Locate every blood parasite and identify its species.
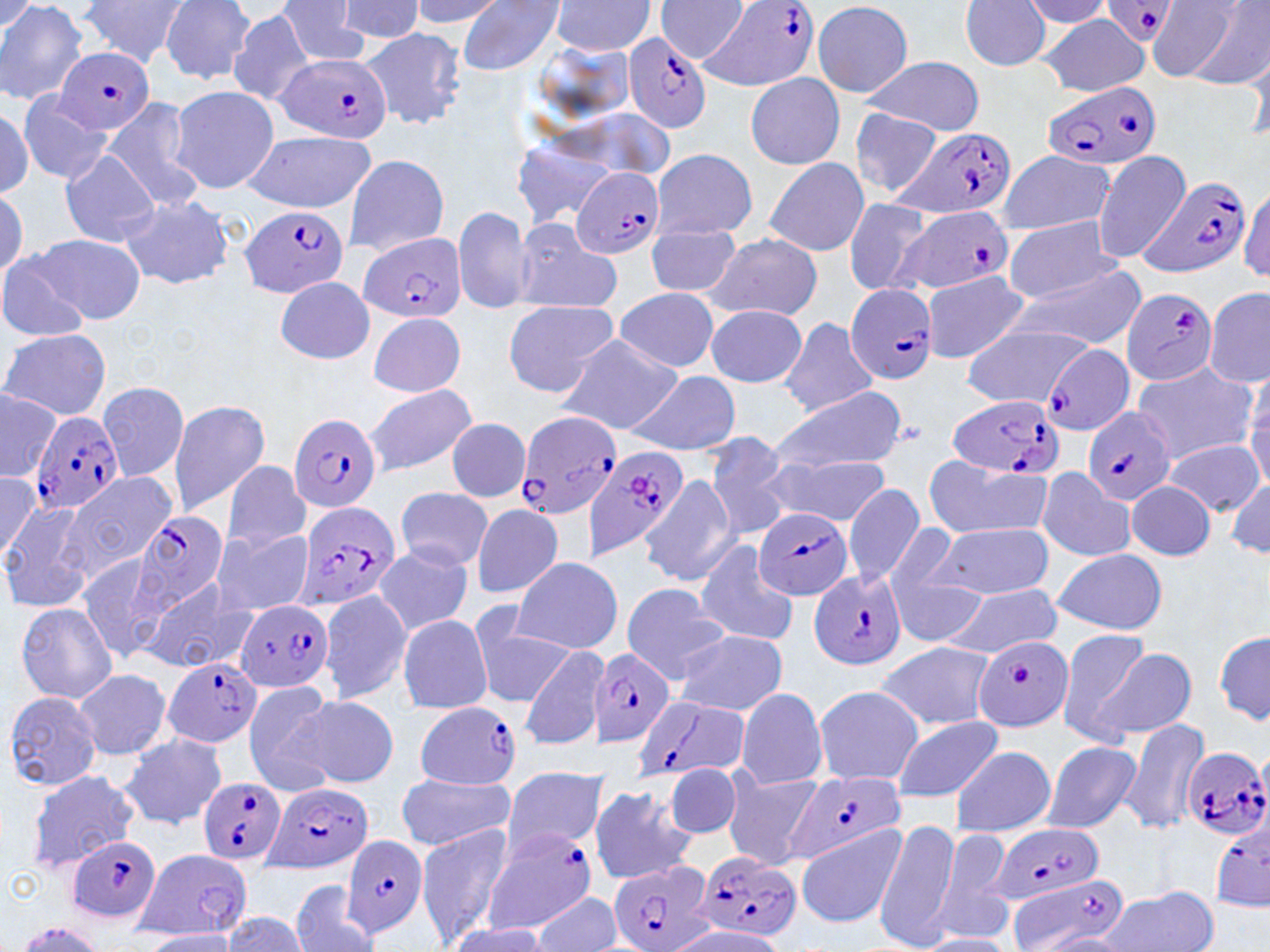

Approximate bounding boxes as [x1, y1, x2, y2] in pixels.
Plasmodium falciparum-infected red blood cells (subset): [697, 0, 821, 92], [1099, 1, 1182, 45], [624, 33, 714, 136], [57, 47, 153, 136], [277, 51, 391, 143], [1041, 83, 1161, 173], [894, 125, 1016, 221], [571, 165, 665, 260], [1141, 177, 1251, 278], [241, 204, 346, 298], [899, 205, 1015, 295], [357, 233, 466, 323], [1121, 289, 1217, 385], [1042, 343, 1135, 435], [947, 394, 1066, 479], [1082, 404, 1175, 506], [513, 409, 623, 522], [28, 412, 124, 517], [288, 413, 381, 515], [581, 446, 691, 559], [290, 500, 401, 614], [756, 507, 852, 601], [128, 509, 230, 611], [807, 568, 907, 673], [234, 600, 331, 692], [974, 636, 1074, 732], [590, 649, 674, 747], [164, 657, 264, 748], [634, 695, 747, 783], [416, 701, 524, 790], [1181, 748, 1270, 840], [788, 772, 910, 861], [196, 777, 288, 865], [263, 781, 375, 874], [1210, 819, 1270, 910], [485, 825, 602, 932], [985, 825, 1105, 905], [64, 834, 162, 924], [341, 835, 429, 938], [136, 848, 253, 940], [689, 850, 803, 942], [609, 857, 716, 952], [1008, 875, 1131, 951].
No Plasmodium ovale, Plasmodium malariae, Plasmodium vivax, Babesia divergens, or Trypanosoma brucei observed.

Uninfected red blood cell locations (subset): [0, 0, 37, 41], [82, 0, 193, 66], [407, 0, 508, 30], [458, 0, 565, 73], [551, 0, 657, 57], [1015, 0, 1116, 31], [1147, 0, 1237, 82], [0, 1, 90, 105], [160, 1, 256, 83], [271, 1, 373, 65], [339, 1, 425, 44], [658, 1, 749, 65], [812, 1, 913, 98], [1188, 1, 1270, 90], [958, 2, 1054, 72], [227, 8, 317, 108], [1037, 14, 1151, 95], [358, 27, 468, 131], [1244, 43, 1270, 145], [861, 57, 988, 135], [745, 72, 845, 170], [167, 86, 279, 193], [18, 91, 113, 184], [100, 96, 201, 205], [0, 107, 33, 195], [552, 107, 676, 179], [850, 108, 945, 197], [244, 131, 377, 214], [512, 136, 621, 227], [649, 148, 758, 240], [59, 150, 160, 247], [996, 150, 1115, 235], [1091, 150, 1190, 263], [342, 153, 452, 259], [762, 157, 868, 257], [1240, 183, 1270, 282], [0, 185, 26, 279], [117, 194, 235, 290], [843, 196, 935, 297], [451, 205, 537, 316], [1003, 218, 1119, 301], [509, 222, 620, 315], [647, 224, 743, 298], [703, 233, 822, 321], [33, 235, 148, 323], [0, 249, 94, 345], [1011, 263, 1147, 350], [922, 271, 1032, 362], [274, 277, 376, 364], [1205, 286, 1270, 389], [614, 287, 719, 372], [501, 300, 619, 397], [706, 303, 807, 387], [367, 311, 467, 396], [778, 316, 878, 417], [961, 324, 1090, 408], [1, 326, 110, 420], [555, 334, 681, 435], [1132, 362, 1256, 462], [628, 371, 739, 455], [96, 381, 189, 484], [364, 383, 477, 476], [770, 386, 907, 472], [0, 387, 62, 481], [1245, 388, 1270, 495], [166, 398, 272, 514], [446, 418, 530, 503], [702, 433, 792, 539], [1160, 440, 1263, 518], [765, 454, 891, 525], [925, 456, 1053, 539], [220, 461, 311, 552], [1034, 466, 1135, 563], [56, 472, 174, 583], [0, 473, 39, 562], [1227, 473, 1270, 562], [639, 475, 739, 585], [1127, 480, 1216, 561], [843, 482, 924, 586], [396, 487, 492, 572], [0, 497, 94, 614], [470, 503, 565, 598], [930, 521, 1051, 600], [211, 530, 315, 618], [693, 539, 800, 647], [886, 539, 985, 644], [373, 546, 473, 636], [1053, 548, 1166, 634], [74, 552, 173, 663], [510, 557, 624, 654], [139, 578, 256, 674], [947, 583, 1061, 656], [620, 584, 729, 683], [318, 588, 412, 704], [15, 602, 118, 705], [467, 610, 578, 707], [397, 611, 494, 710], [1214, 628, 1269, 726], [1054, 629, 1151, 746], [672, 630, 788, 715], [876, 641, 996, 729], [518, 644, 608, 753], [1093, 647, 1197, 738], [73, 669, 170, 760], [241, 681, 341, 794], [812, 685, 926, 786], [736, 687, 829, 790], [5, 690, 100, 791], [297, 695, 399, 788], [888, 715, 1005, 802], [1118, 716, 1209, 835], [120, 734, 226, 830], [1041, 740, 1140, 834], [951, 747, 1056, 838], [664, 760, 745, 841], [498, 766, 608, 859], [721, 768, 825, 870], [25, 771, 137, 872], [395, 771, 513, 852], [588, 784, 697, 884], [820, 802, 945, 943], [874, 819, 960, 949], [417, 824, 516, 946], [796, 826, 906, 927], [934, 828, 1012, 938], [290, 882, 381, 952], [1098, 887, 1218, 952], [530, 891, 620, 951], [219, 912, 309, 952], [13, 921, 106, 951], [444, 923, 552, 952], [670, 927, 787, 952], [136, 930, 241, 952], [917, 933, 1016, 952]. Slide-level diagnosis: Plasmodium falciparum. Light microscopy. One field of a larger specimen. Image is 1270×952 pixels. Thin blood film. 1000x magnification. May-Grünwald-Giemsa-stained preparation.